Locate and identify every blood parasite.
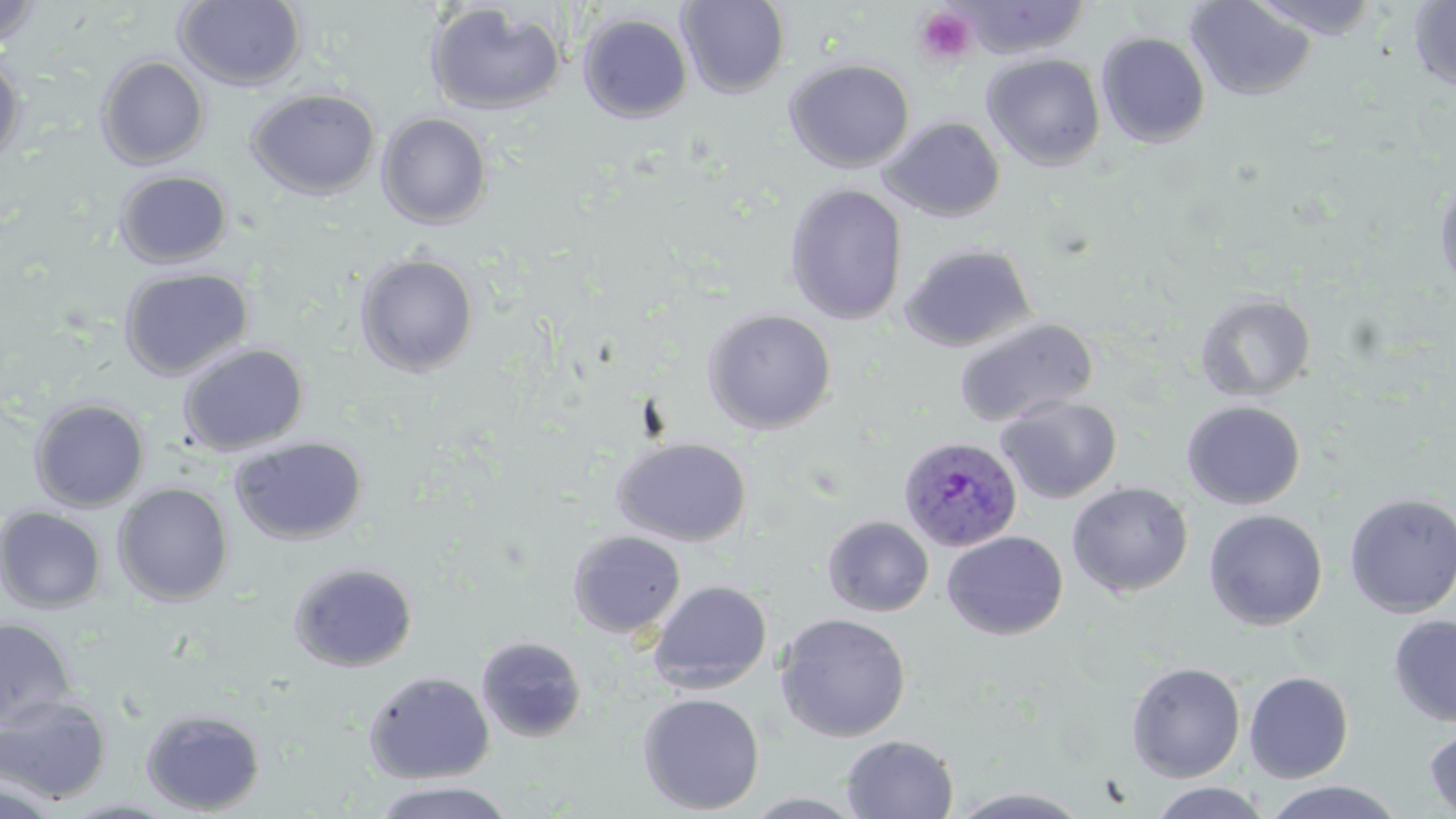

Approximate bounding boxes as named x1/y1/x2/y2 corners in pixels.
Plasmodium ovale-infected red blood cells: (x1=898, y1=435, x2=1023, y2=552).
No Plasmodium falciparum, Plasmodium malariae, Plasmodium vivax, Babesia divergens, or Trypanosoma brucei observed.

slide_level_diagnosis: Plasmodium ovale
field_of_view: one of a larger specimen
preparation: thin blood film
stain: May-Grünwald-Giemsa
uninfected_red_blood_cell_locations: 'approximate bounding boxes as named x1/y1/x2/y2 corners in pixels: (x1=174, y1=0, x2=307, y2=91), (x1=677, y1=0, x2=790, y2=99), (x1=1245, y1=0, x2=1385, y2=40), (x1=0, y1=1, x2=45, y2=52), (x1=955, y1=1, x2=1091, y2=59), (x1=1185, y1=1, x2=1316, y2=100), (x1=1408, y1=1, x2=1456, y2=93), (x1=425, y1=3, x2=567, y2=116), (x1=577, y1=13, x2=693, y2=123), (x1=1096, y1=31, x2=1211, y2=147), (x1=0, y1=52, x2=25, y2=164), (x1=982, y1=53, x2=1105, y2=170), (x1=96, y1=55, x2=210, y2=169), (x1=784, y1=58, x2=915, y2=173), (x1=246, y1=88, x2=380, y2=199), (x1=376, y1=112, x2=493, y2=229), (x1=879, y1=115, x2=1005, y2=222), (x1=114, y1=170, x2=233, y2=268), (x1=1434, y1=172, x2=1456, y2=300), (x1=784, y1=183, x2=908, y2=325), (x1=899, y1=243, x2=1036, y2=353), (x1=355, y1=253, x2=479, y2=377), (x1=118, y1=268, x2=253, y2=380), (x1=1195, y1=292, x2=1317, y2=402), (x1=139, y1=297, x2=294, y2=418), (x1=702, y1=308, x2=837, y2=434), (x1=953, y1=316, x2=1098, y2=428), (x1=177, y1=342, x2=309, y2=456), (x1=996, y1=396, x2=1122, y2=503), (x1=29, y1=398, x2=150, y2=512), (x1=1181, y1=400, x2=1306, y2=509), (x1=229, y1=436, x2=368, y2=545), (x1=612, y1=437, x2=752, y2=547), (x1=1067, y1=482, x2=1193, y2=597), (x1=112, y1=483, x2=234, y2=606), (x1=1343, y1=492, x2=1456, y2=618), (x1=1, y1=507, x2=106, y2=613), (x1=1203, y1=509, x2=1328, y2=630), (x1=823, y1=515, x2=934, y2=617), (x1=568, y1=531, x2=686, y2=638), (x1=942, y1=531, x2=1068, y2=640), (x1=288, y1=561, x2=418, y2=672), (x1=648, y1=580, x2=772, y2=693), (x1=774, y1=612, x2=911, y2=742), (x1=1389, y1=614, x2=1456, y2=728), (x1=0, y1=618, x2=76, y2=730), (x1=477, y1=636, x2=587, y2=742), (x1=1126, y1=661, x2=1246, y2=783), (x1=363, y1=670, x2=494, y2=784), (x1=1244, y1=671, x2=1354, y2=783), (x1=637, y1=692, x2=765, y2=815), (x1=0, y1=694, x2=113, y2=804), (x1=140, y1=707, x2=266, y2=815), (x1=1423, y1=722, x2=1456, y2=818), (x1=841, y1=735, x2=959, y2=818), (x1=2, y1=776, x2=63, y2=818), (x1=370, y1=780, x2=518, y2=819), (x1=1260, y1=780, x2=1407, y2=818), (x1=1147, y1=782, x2=1275, y2=818), (x1=946, y1=787, x2=1096, y2=818), (x1=742, y1=792, x2=871, y2=818)'
modality: light microscopy
platelet_locations: 'approximate bounding boxes as named x1/y1/x2/y2 corners in pixels: (x1=913, y1=6, x2=979, y2=67)'
image_size: 1456×819 pixels
magnification: 1000x